Evaluate for Plasmodium parasites.
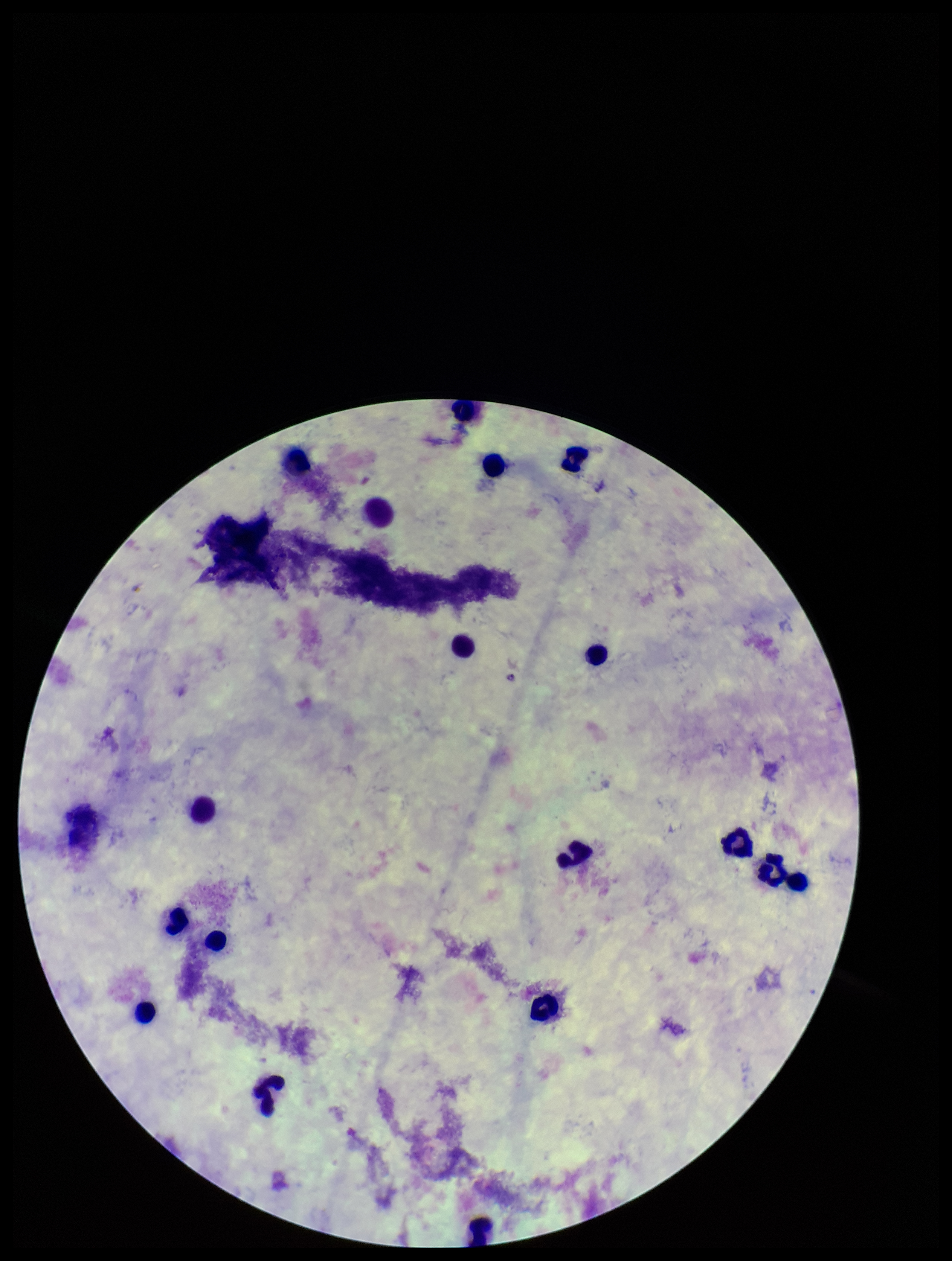
None detected.

patient malaria status = negative
parasite count = 0
capture = smartphone photograph through the microscope eyepiece
preparation = thick blood smear
leukocyte count = 18
image size = 952×1261 pixels
stain = Giemsa
field of view = single